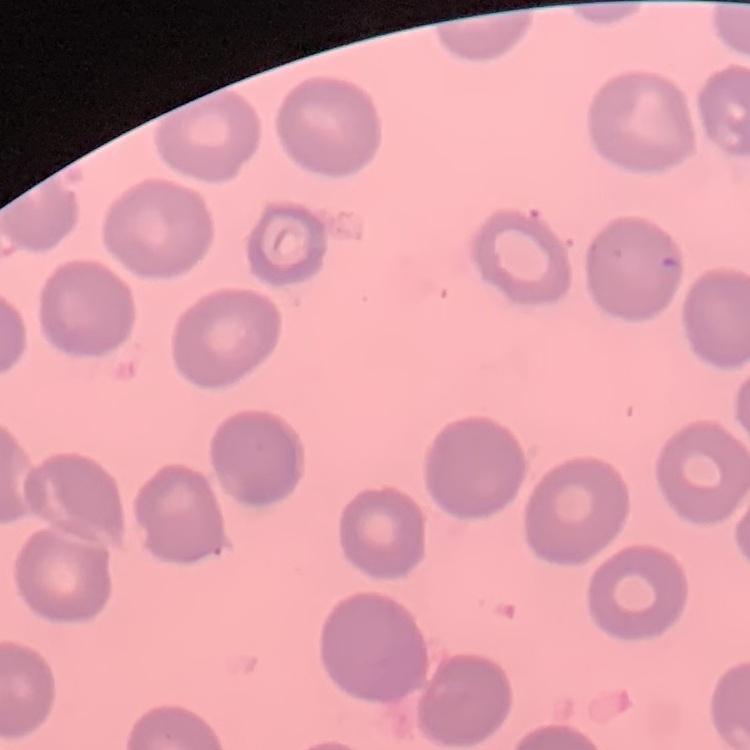
The red blood cells show no rouleaux formation. Thin blood smear. Square crop of a larger photomicrograph. Field's or Giemsa stain.